Assess for Plasmodium parasites.
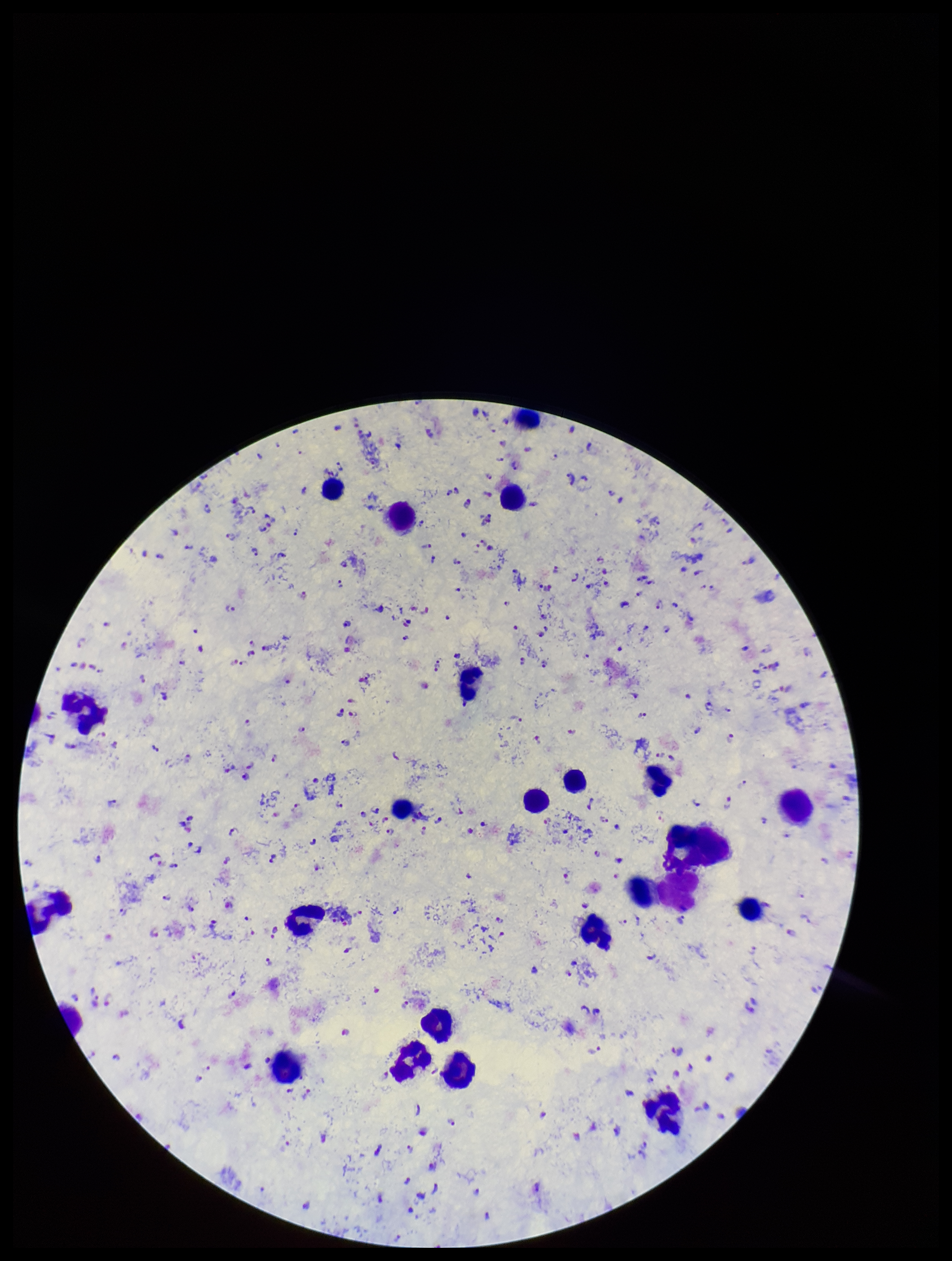
Detected.

field_of_view: one from this slide
capture: smartphone photograph through the microscope eyepiece
image_size: 952×1261 pixels
stain: Giemsa
species_reported_for_this_patient: Plasmodium falciparum
leukocyte_count: 23
parasite_count: 247
patient_malaria_status: infected
preparation: thick smear